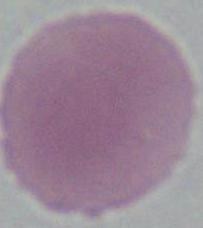
Summary:
  - Magnification: 1000x
  - Identification: red blood cell
  - Modality: micrograph